Describe the morphology of the red blood cells.
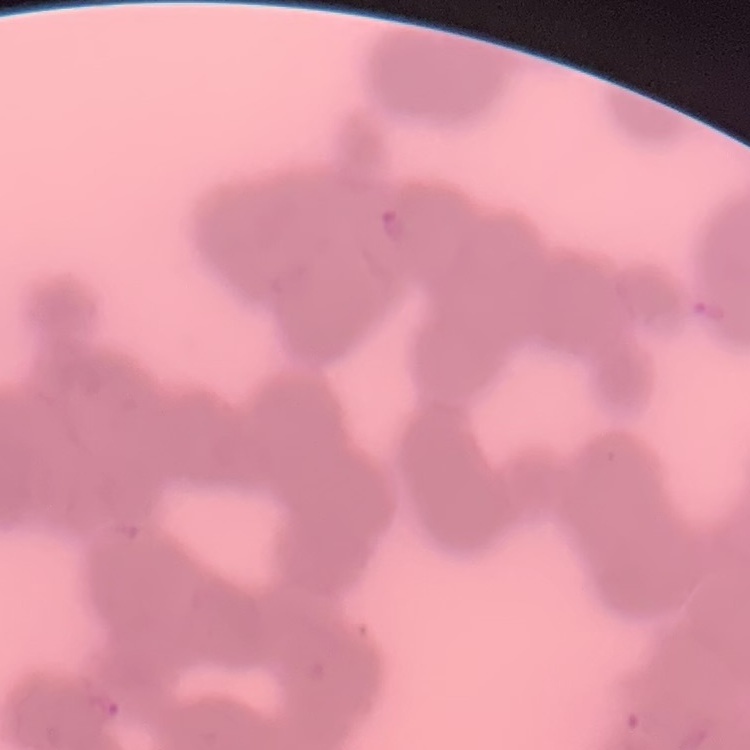
Rouleaux formation.

preparation = thin blood smear
image type = square crop of a larger photomicrograph
stain = Field's or Giemsa